Identify the cell.
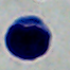

A leukocyte.

1000x magnification. Micrograph.